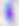
modality: photomicrograph
identification: Toxoplasma gondii
magnification: 400x